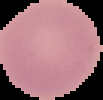 From a thin blood film. Image is 103×100 pixels. Malaria status: uninfected. Segmented cell region on a black background.